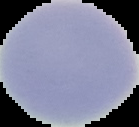
{
  "malaria_status": "uninfected",
  "image_size": "139×127 pixels",
  "image_type": "segmented cell region on a black background",
  "preparation": "thin blood smear"
}